Describe the morphology of the erythrocytes.
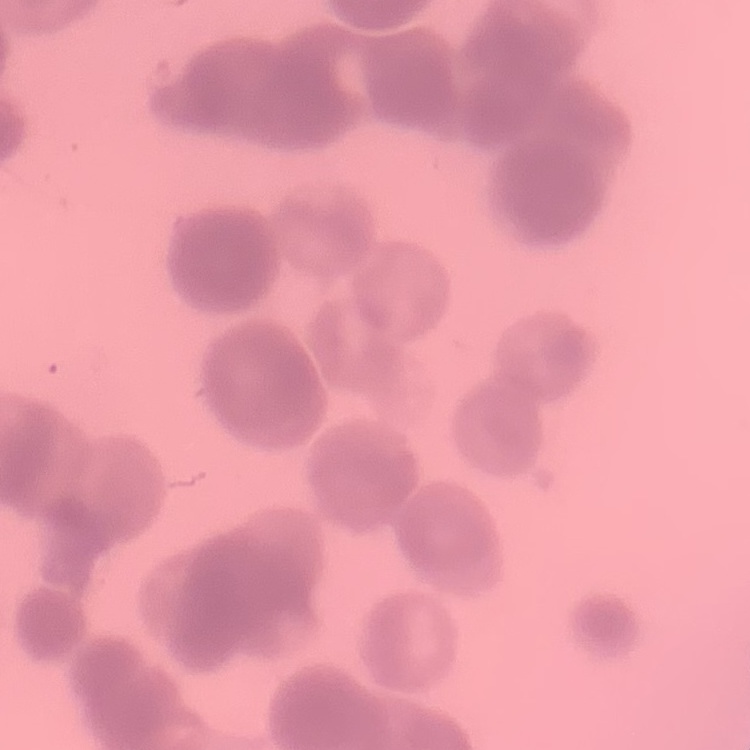
They show rouleaux formation.

Summary:
  - Stain: Field's or Giemsa
  - Image type: square crop of a larger photomicrograph
  - Preparation: thin blood film